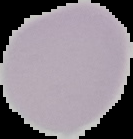

Summary:
  - Image size: 133×139 pixels
  - Image type: cell region segmented out of the field of view; surrounding area masked to black
  - Malaria status: uninfected
  - Preparation: thin blood smear